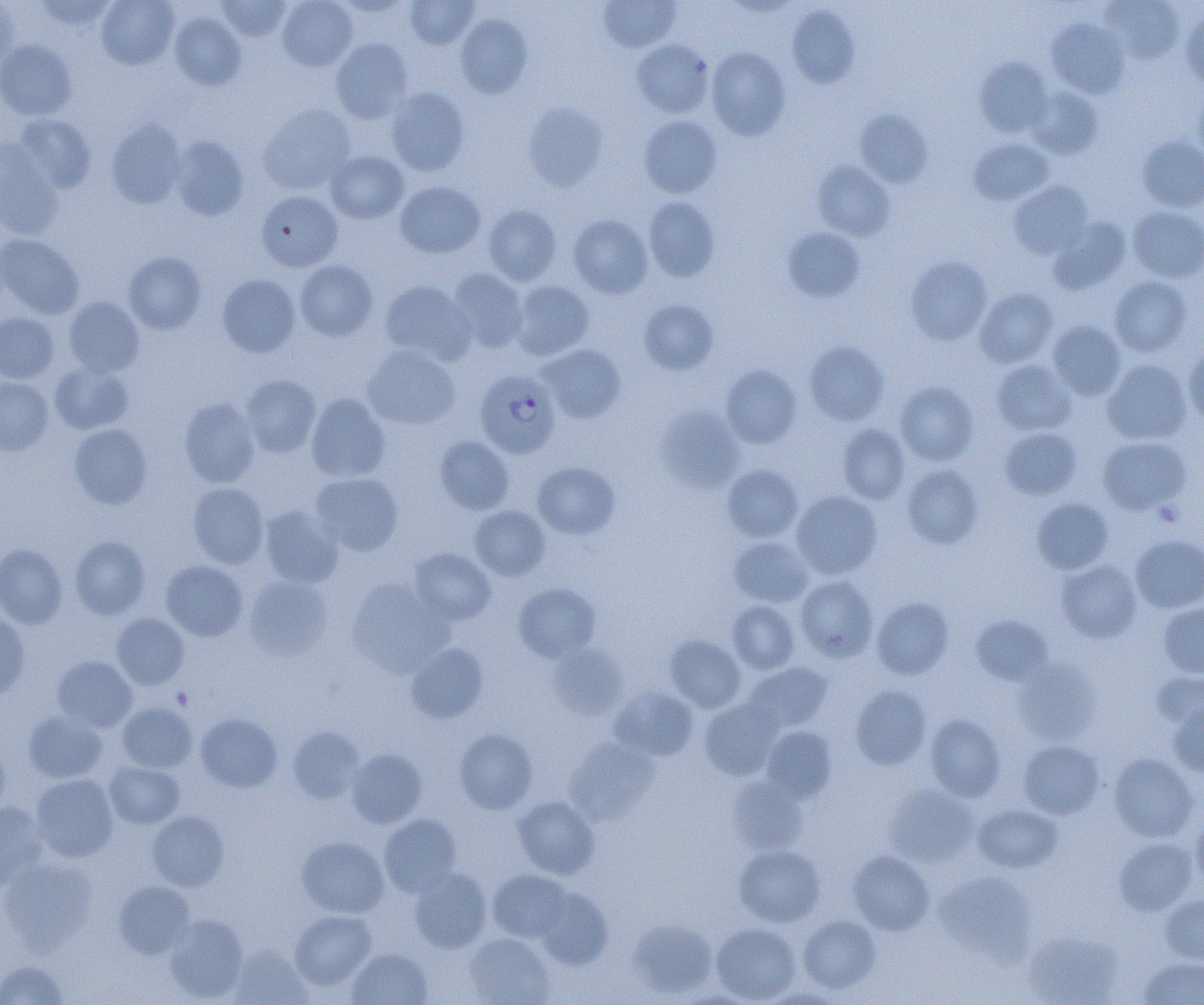
Summary:
  - Coordinate format: approximate bounding boxes as [x1, y1, x2, y2] in pixels
  - Plasmodium falciparum-infected red blood cell locations: [474, 370, 561, 459]
  - Uninfected red blood cell locations: [33, 0, 119, 32], [96, 0, 179, 70], [215, 0, 293, 42], [277, 0, 357, 71], [405, 0, 479, 49], [597, 0, 681, 52], [0, 1, 18, 68], [1103, 1, 1184, 64], [786, 5, 860, 88], [1181, 9, 1204, 90], [169, 11, 246, 90], [456, 14, 533, 98], [1046, 18, 1130, 98], [330, 38, 413, 124], [0, 40, 78, 121], [632, 40, 713, 117], [706, 46, 791, 140], [975, 58, 1053, 137], [1028, 87, 1105, 159], [385, 88, 469, 176], [1193, 91, 1204, 167], [523, 102, 608, 191], [259, 104, 356, 194], [855, 109, 933, 188], [14, 114, 96, 193], [638, 116, 722, 198], [106, 120, 186, 208], [168, 135, 249, 221], [1137, 136, 1204, 212], [968, 137, 1054, 205], [0, 138, 63, 239], [324, 150, 409, 224], [812, 161, 896, 241], [1009, 180, 1093, 259], [395, 181, 486, 258], [256, 190, 343, 272], [643, 196, 720, 281], [483, 204, 561, 286], [1128, 206, 1204, 282], [567, 214, 653, 298], [1049, 217, 1131, 293], [782, 227, 865, 302], [0, 234, 84, 319], [123, 252, 207, 334], [906, 256, 992, 346], [294, 260, 378, 341], [446, 268, 529, 353], [217, 274, 301, 357], [1109, 276, 1192, 357], [379, 279, 474, 364], [510, 280, 595, 360], [975, 287, 1058, 367], [62, 297, 145, 377], [639, 299, 719, 374], [0, 313, 59, 383], [1048, 320, 1126, 400], [804, 341, 890, 426], [538, 344, 626, 424], [1183, 344, 1204, 427], [361, 345, 461, 430], [1102, 359, 1191, 445], [991, 360, 1076, 435], [50, 362, 134, 434], [720, 365, 803, 449], [239, 375, 321, 458], [0, 377, 53, 456], [895, 381, 978, 465], [306, 393, 390, 482], [179, 397, 260, 488], [656, 404, 745, 493], [69, 423, 153, 509], [837, 424, 910, 504], [999, 427, 1082, 500], [434, 436, 514, 515], [1097, 436, 1191, 514], [532, 462, 620, 539], [721, 464, 804, 542], [902, 464, 984, 549], [310, 472, 404, 555], [187, 482, 269, 568], [791, 490, 882, 579], [1031, 497, 1114, 574], [259, 505, 343, 589], [470, 505, 551, 581], [70, 535, 150, 619], [1131, 535, 1204, 613], [728, 536, 813, 607], [0, 543, 68, 629], [409, 548, 496, 624], [1056, 558, 1142, 643], [160, 560, 248, 641], [243, 575, 334, 660], [795, 575, 878, 662], [346, 580, 452, 677], [513, 583, 601, 662], [872, 597, 954, 679], [726, 600, 801, 674], [1158, 603, 1204, 679], [0, 613, 30, 701], [111, 613, 190, 690], [970, 614, 1053, 686], [665, 634, 746, 712], [406, 642, 489, 723], [546, 642, 629, 720], [52, 655, 137, 731], [1014, 659, 1102, 745], [742, 661, 834, 733], [1151, 671, 1204, 731], [850, 684, 932, 770], [610, 686, 699, 760], [699, 697, 784, 780], [1167, 700, 1204, 777], [116, 702, 197, 772], [23, 711, 108, 784], [195, 712, 282, 792], [925, 714, 1006, 802], [288, 725, 365, 803], [761, 726, 837, 802], [454, 728, 538, 813], [565, 736, 659, 823], [0, 740, 10, 820], [1018, 740, 1105, 819], [346, 748, 427, 828], [1108, 752, 1200, 842], [104, 761, 185, 829], [31, 774, 118, 862], [728, 776, 808, 855], [884, 783, 980, 867], [512, 795, 600, 879], [0, 801, 47, 888], [973, 803, 1062, 873], [147, 810, 229, 890], [1191, 811, 1204, 893], [379, 814, 461, 897], [296, 836, 389, 918], [1113, 837, 1197, 915], [734, 844, 825, 927], [847, 850, 934, 935], [0, 857, 99, 953], [409, 867, 492, 953], [488, 869, 572, 943], [934, 871, 1037, 962], [114, 880, 195, 959], [533, 886, 612, 969], [1160, 894, 1204, 964], [289, 910, 376, 990], [164, 915, 248, 1002], [799, 915, 881, 994], [629, 918, 718, 998], [711, 923, 801, 1003], [1023, 930, 1123, 1005], [464, 932, 555, 1004], [229, 944, 312, 1004], [347, 948, 432, 1005], [1138, 956, 1204, 1004], [0, 958, 69, 1005]
  - Platelet locations: [1153, 500, 1184, 526]
  - Slide-level diagnosis: Plasmodium falciparum
  - Modality: optical microscopy
  - Magnification: 1000x
  - Preparation: thin blood smear
  - Field of view: one of a larger specimen
  - Image size: 1204×1005 pixels